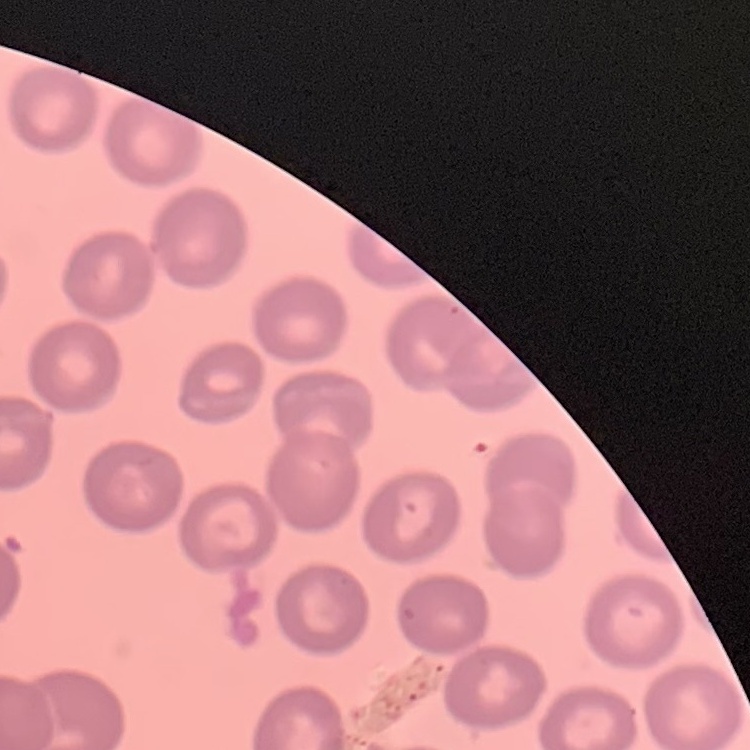
The red blood cells show no rouleaux formation. Field's or Giemsa stain. Thin peripheral smear. Square crop of a larger photomicrograph.